Comment on the morphology of the erythrocytes.
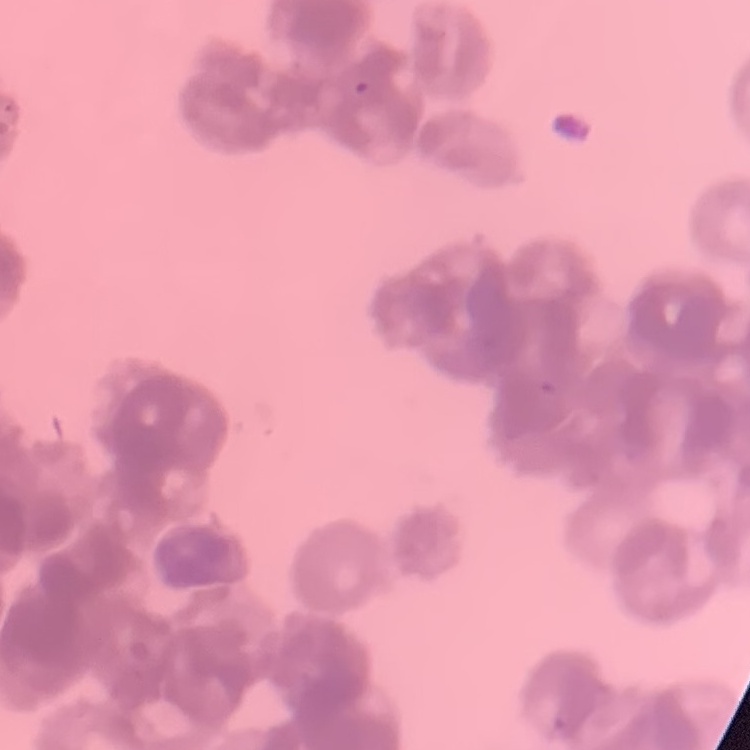
They show rouleaux formation.

One tile cut from a larger photomicrograph. Thin peripheral smear. Stained with either Field's or Giemsa.